State which parasite is depicted.
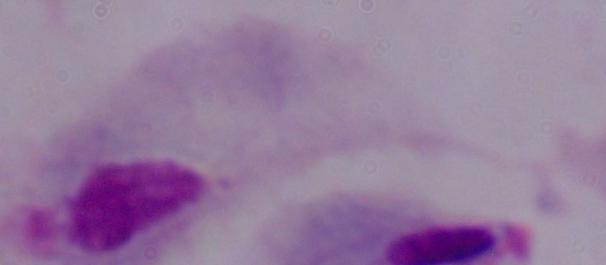
A trichomonad.

Micrograph. Captured at 1000x magnification.